Assess this cell for malaria.
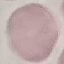
It is uninfected.

{
  "capture": "smartphone through the microscope eyepiece",
  "stain": "Giemsa",
  "image_type": "cell patch, automatically extracted from a larger field of view and resized to 64 × 64 pixels",
  "preparation": "thin blood smear"
}